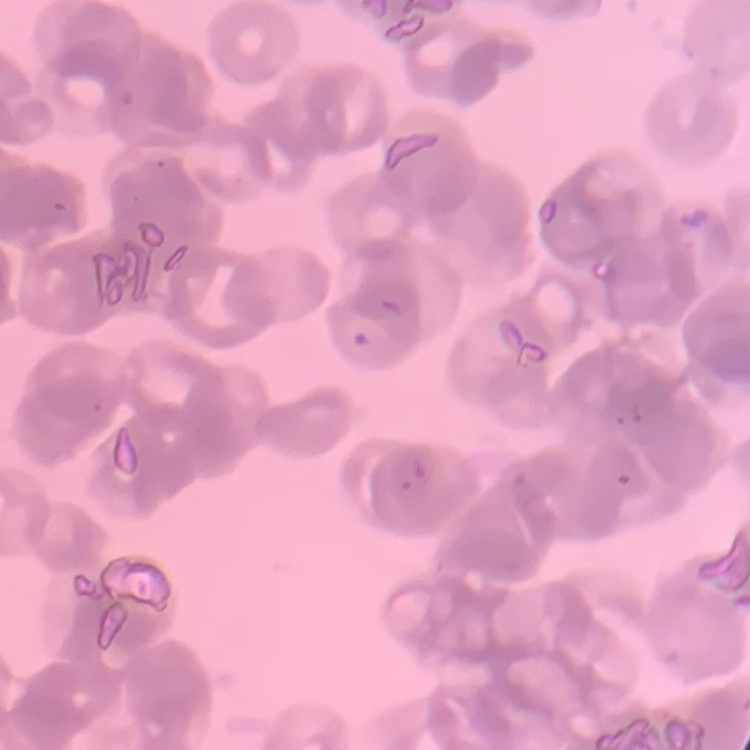
red_blood_cell_morphology: rouleaux formation
preparation: thin peripheral smear
stain: Field's or Giemsa
image_type: square crop of a larger photomicrograph